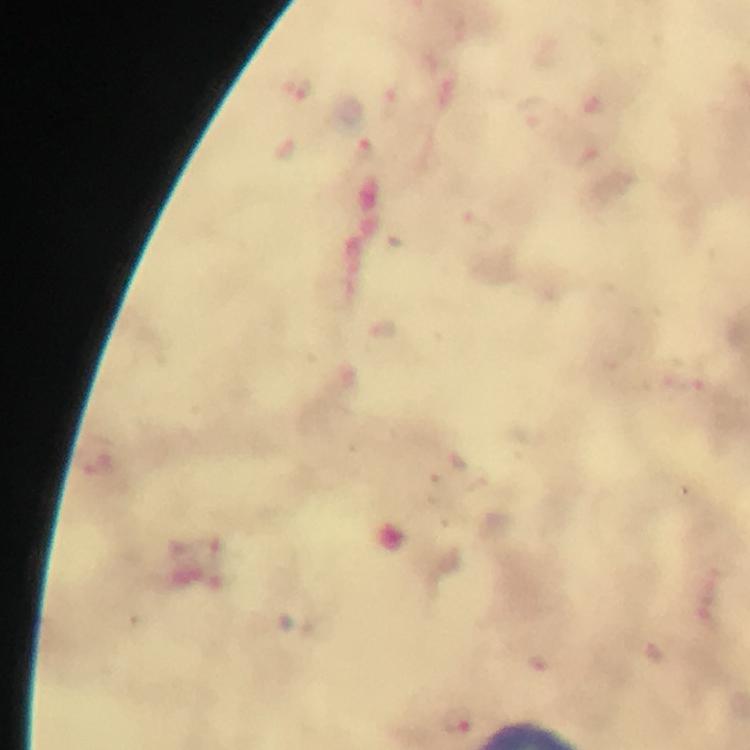
Approximate centers as (x, y) in pixels. Plasmodium parasite locations: (302, 89), (365, 149), (458, 720). Thick smear. Photographed with a smartphone mounted on the microscope. 100x magnification. Immersion oil was used. From a diagnostic examination for malaria. A crop from one field of view. Image is 750×750 pixels. Giemsa stain.